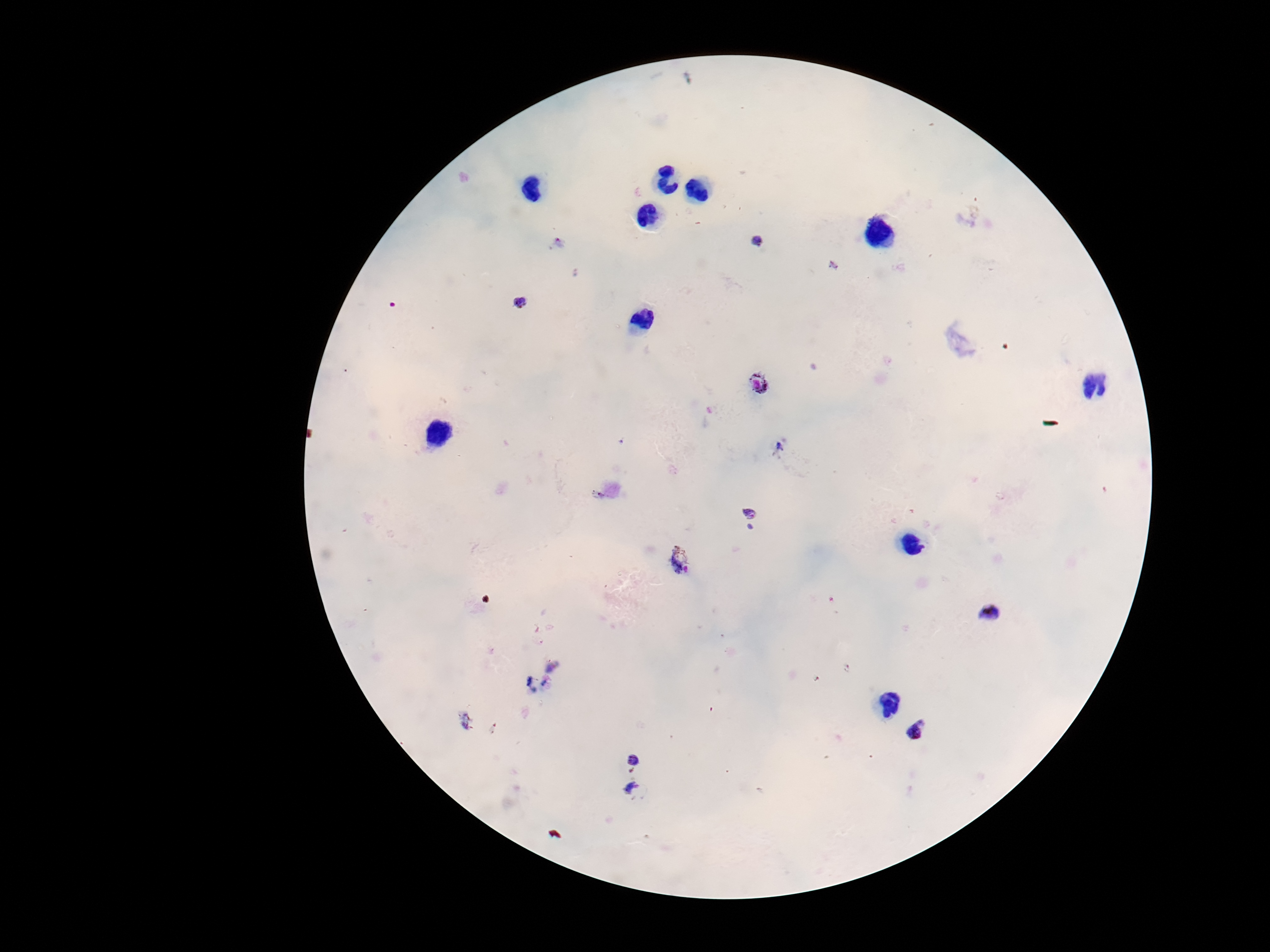

field_of_view: one from this slide
preparation: thick peripheral-blood smear
stain: Giemsa
plasmodium_parasite_locations: 'approximate centers as {x, y} in pixels: {758, 243}, {521, 304}, {759, 386}, {780, 450}, {751, 514}, {679, 563}, {993, 613}, {535, 683}, {466, 722}, {917, 732}, {632, 756}, {633, 792}'
capture: smartphone camera through the microscope eyepiece
patient_malaria_status: infected
image_size: 1270×952 pixels
magnification: 100x